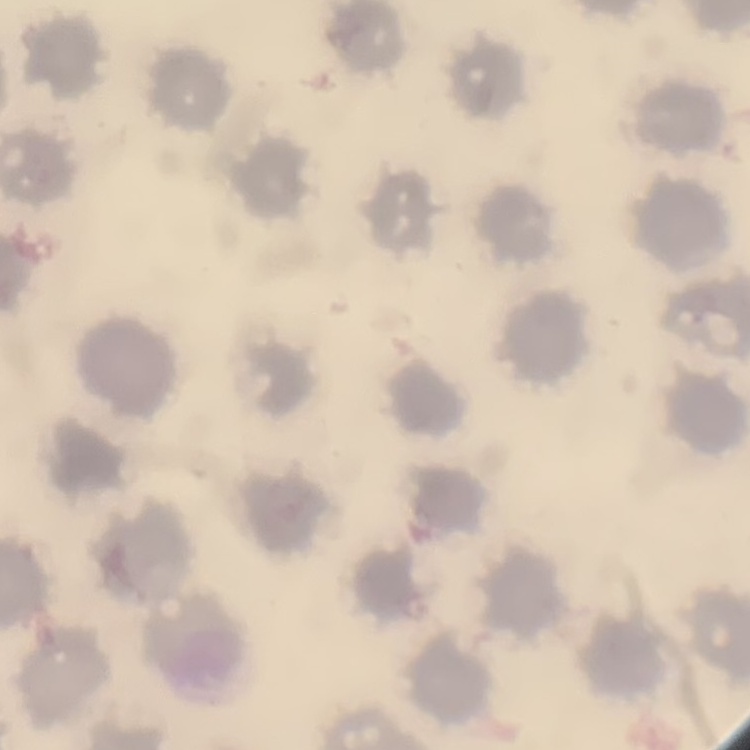

Summary:
  - Erythrocyte morphology: no rouleaux formation
  - Preparation: thin blood smear
  - Image type: one tile cut from a larger photomicrograph
  - Stain: Field's or Giemsa